Assess for malaria.
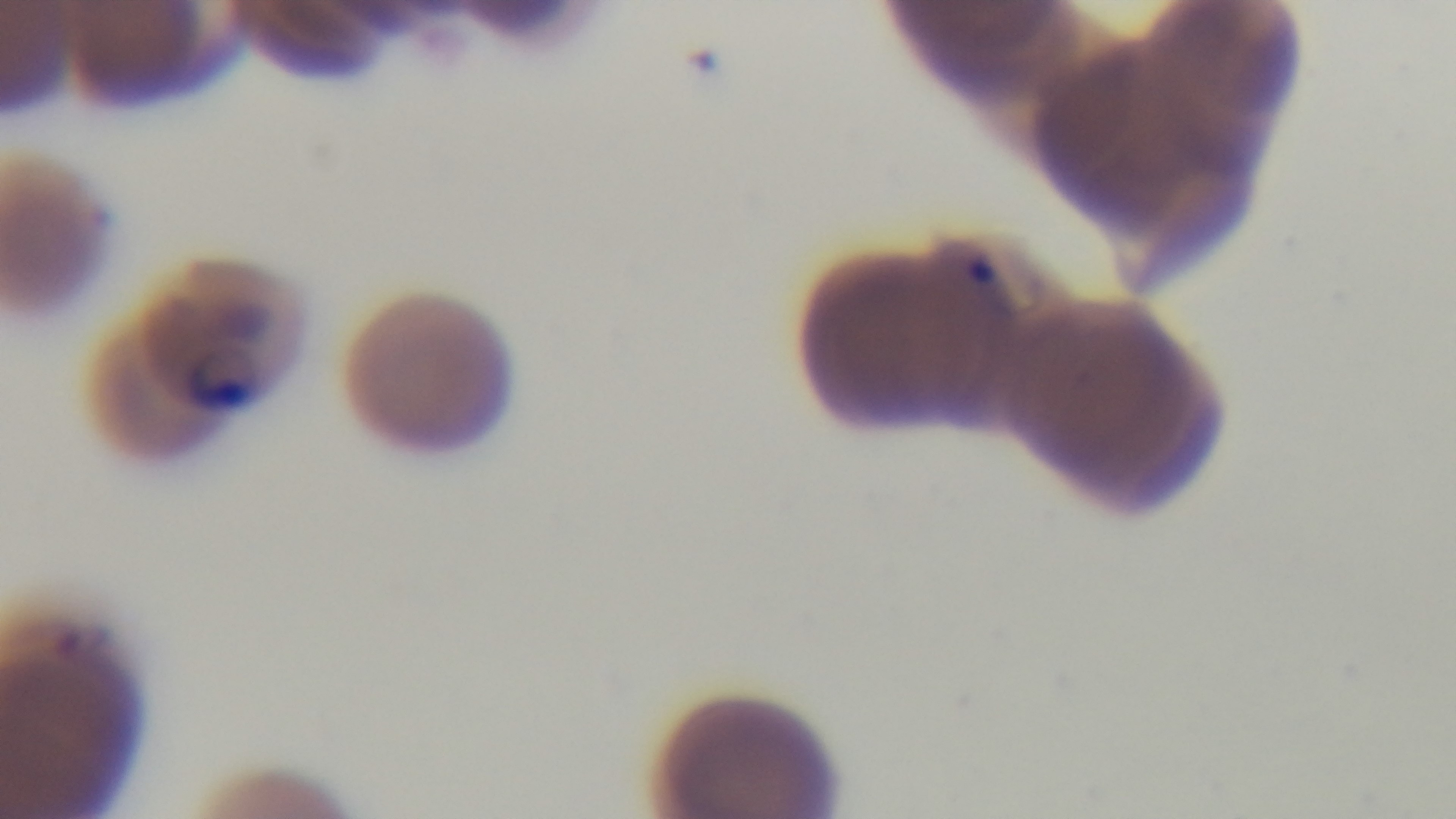
Infected.

Summary:
  - Stain: Giemsa
  - Modality: light microscopy
  - Capture: mounted 4K digital camera
  - Objective: 100x oil immersion
  - Field of view: single
  - Preparation: thin blood film